Point out each Plasmodium parasite.
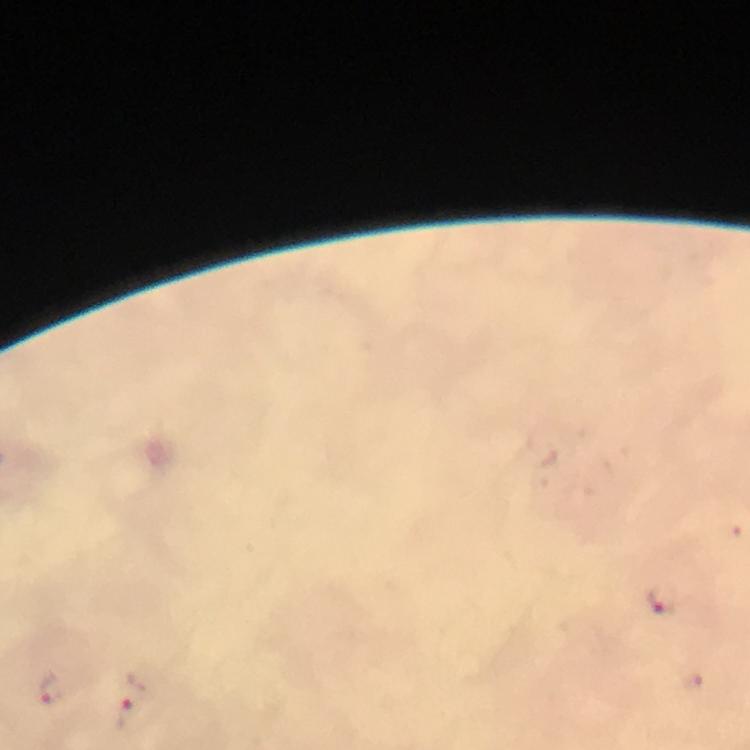

Approximate centers as {x, y} in pixels.
Plasmodium parasites: {664, 600}, {690, 680}, {52, 687}, {132, 702}.

Immersion oil applied. Image is 750×750 pixels. Thick smear. Photographed with a smartphone mounted on the microscope. From a malaria diagnostic workup. At 100x magnification. Cropped region of a single field of view. Giemsa-stained preparation.